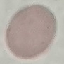
Malaria status: uninfected. Photographed with a smartphone camera at the microscope eyepiece. Thin smear of blood. Giemsa-stained preparation. Automatically extracted cell patch, resized to 64 × 64 pixels.